Assess the morphology of the erythrocytes.
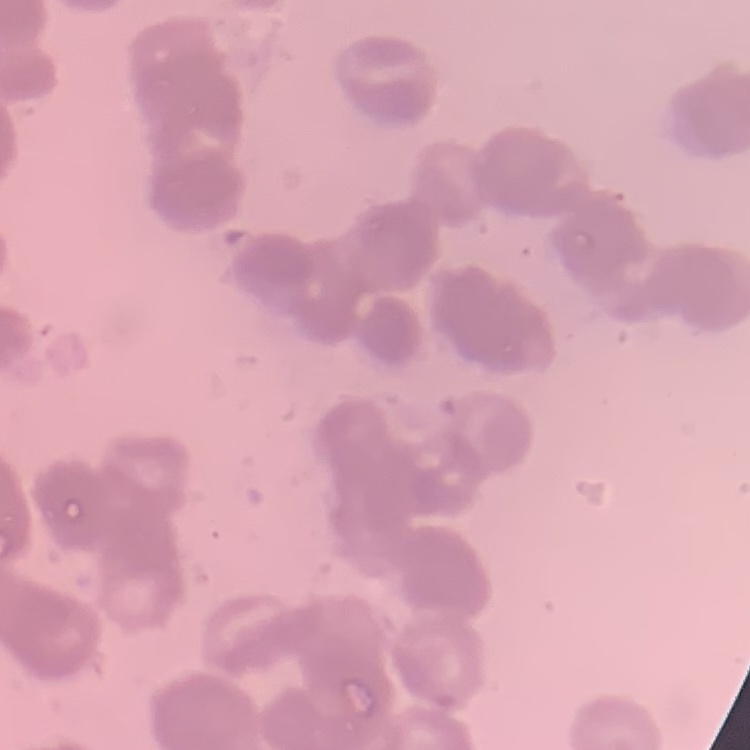

They show rouleaux formation.

stain = Field's or Giemsa
image type = one tile cut from a larger photomicrograph
preparation = thin blood smear